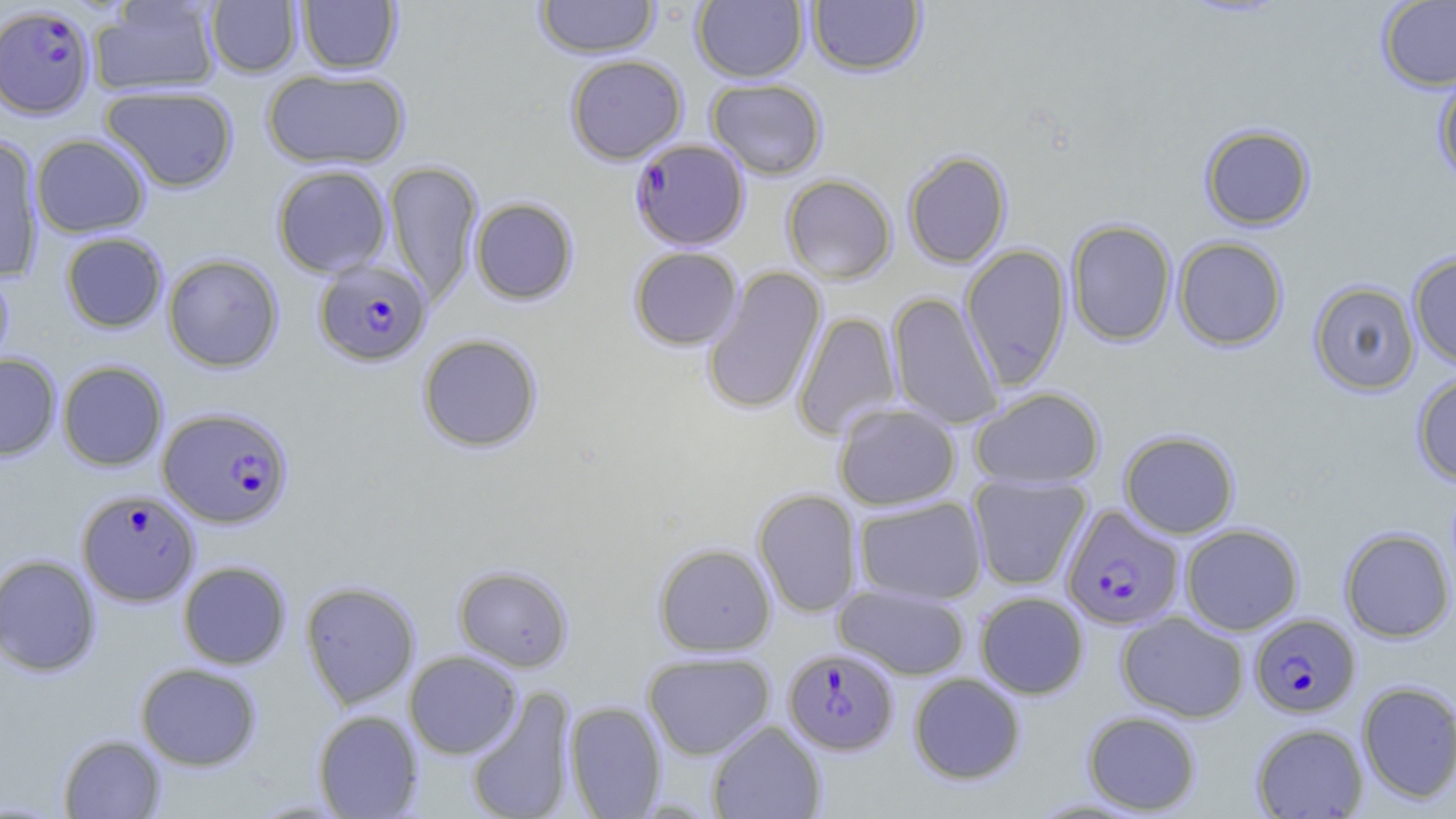 Approximate bounding boxes as (x1, y1, x2, y2) in pixels. Uninfected red blood cell locations: (89, 0, 222, 97), (535, 0, 660, 59), (692, 0, 808, 82), (1377, 0, 1456, 91), (206, 1, 302, 77), (296, 1, 402, 74), (806, 1, 927, 77), (565, 54, 688, 164), (262, 68, 410, 171), (1433, 71, 1456, 188), (706, 78, 827, 179), (100, 85, 239, 193), (1200, 124, 1315, 231), (0, 134, 44, 283), (30, 134, 151, 237), (903, 151, 1012, 268), (383, 160, 484, 307), (271, 164, 392, 277), (782, 174, 897, 284), (470, 197, 579, 305), (1065, 219, 1177, 346), (59, 232, 168, 333), (1173, 237, 1288, 351), (960, 244, 1072, 389), (628, 247, 743, 350), (1407, 252, 1456, 370), (162, 253, 284, 372), (0, 266, 14, 377), (701, 266, 827, 416), (1309, 281, 1420, 395), (887, 292, 1003, 429), (792, 311, 902, 441), (416, 334, 543, 453), (0, 353, 61, 460), (57, 360, 168, 471), (1411, 370, 1456, 486), (970, 387, 1105, 490), (833, 403, 961, 510), (1119, 429, 1240, 538), (968, 472, 1092, 590), (752, 488, 862, 617), (853, 496, 988, 604), (1180, 523, 1303, 635), (1339, 527, 1455, 642), (653, 543, 777, 656), (0, 554, 102, 677), (178, 561, 291, 669), (453, 564, 574, 671), (300, 580, 421, 709), (834, 584, 971, 680), (974, 591, 1089, 699), (1116, 612, 1249, 722), (404, 651, 523, 758), (643, 652, 775, 760), (135, 662, 262, 770), (908, 672, 1026, 785), (1356, 681, 1456, 804), (465, 685, 578, 819), (564, 701, 667, 817), (312, 709, 423, 818), (1082, 710, 1201, 815), (707, 720, 827, 819), (1251, 723, 1369, 818), (57, 733, 167, 818). Plasmodium falciparum-infected red blood cell locations: (0, 5, 95, 121), (630, 138, 750, 251), (313, 258, 433, 366), (158, 406, 293, 529), (76, 489, 200, 606), (1061, 504, 1185, 631), (1249, 613, 1360, 718), (783, 647, 898, 755). Slide-level diagnosis: Plasmodium falciparum. Image is 1456×819 pixels. Light microscopy. Thin blood smear. Single field of view. May-Grünwald-Giemsa stain. 1000x magnification.